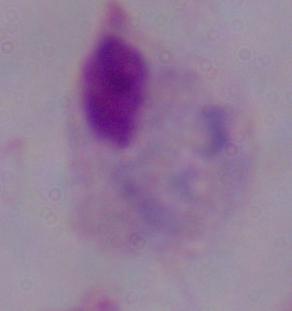

Summary:
  - Modality: micrograph
  - Identification: trichomonad
  - Magnification: 1000x